Outline each P. falciparum parasite and classify it by life-cycle stage.
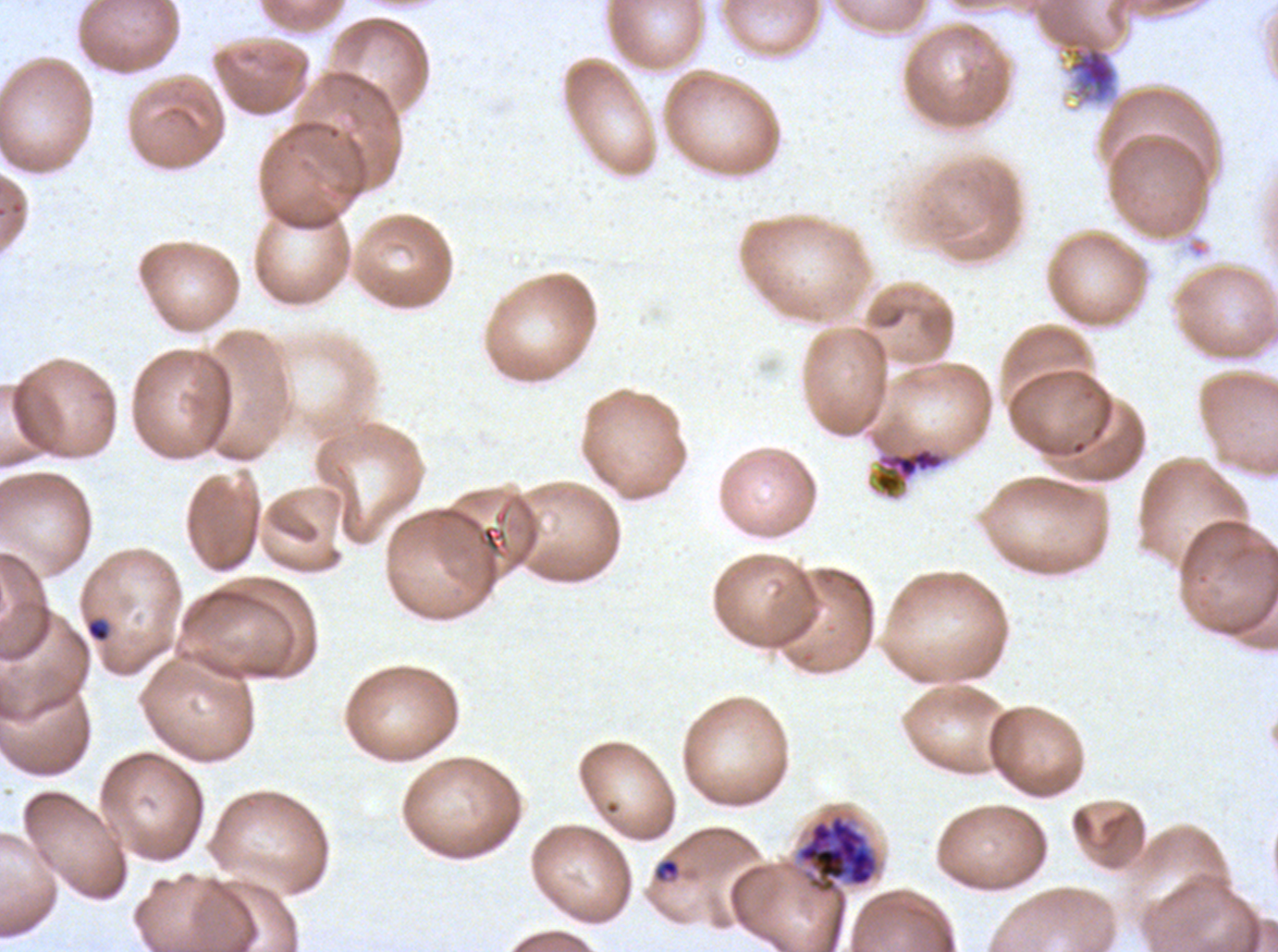

Approximate bounding rectangles given as corner coordinates in pixels from the top-left.
Rings: (x1=86, y1=618, x2=110, y2=642), (x1=653, y1=857, x2=681, y2=884).
Late schizonts: (x1=795, y1=813, x2=879, y2=894).
No late-ring/early-trophozoite forms, mid trophozoites, late trophozoites, early schizonts, segmenters, or gametocytes observed.

Summary:
  - Debris locations: (x1=1063, y1=36, x2=1117, y2=102), (x1=871, y1=445, x2=949, y2=501)
  - Field of view: sub-image separated from a larger composite
  - Life-cycle stages observed: ring, late schizont
  - Specimen: P. falciparum cultured ex vivo for 24 to 48 hours, from a patient in The Gambia
  - Image size: 1278×952 pixels
  - Preparation: thin blood film
  - Stain: Giemsa